Assess the morphology of the erythrocytes.
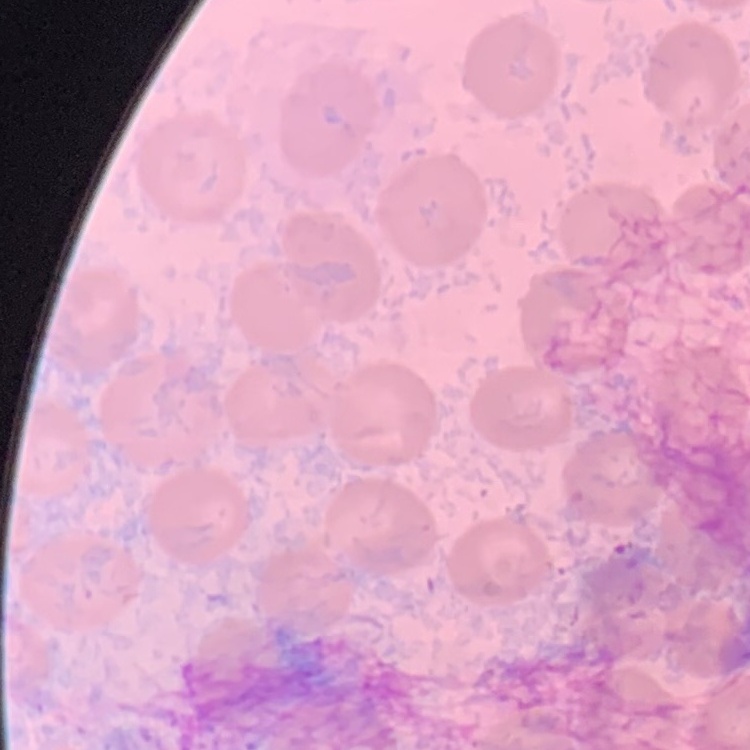

They show no rouleaux formation.

Summary:
  - Image type: one tile cut from a larger photomicrograph
  - Stain: Field's or Giemsa
  - Preparation: thin blood film